Locate malaria parasites and leukocytes.
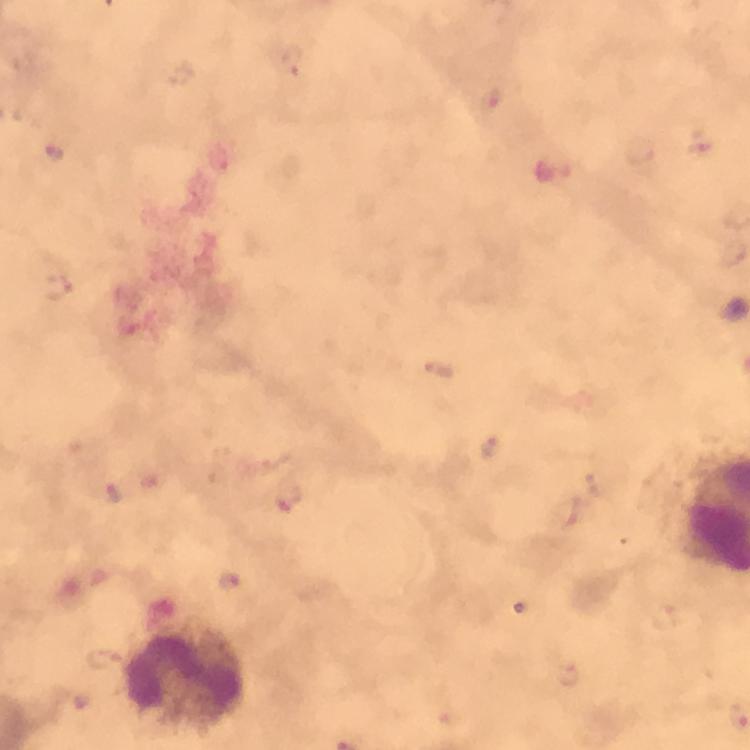

Approximate centers as {x, y} in pixels.
Malaria parasites: {294, 59}, {55, 154}, {115, 493}, {286, 499}, {570, 675}.
Leukocytes: {185, 675}.

capture = smartphone camera through the microscope
stain = Giemsa
magnification = 100x
image size = 750×750 pixels
preparation = thick smear
context = from a diagnostic examination for malaria
cropped from = a single field of view
immersion oil = applied